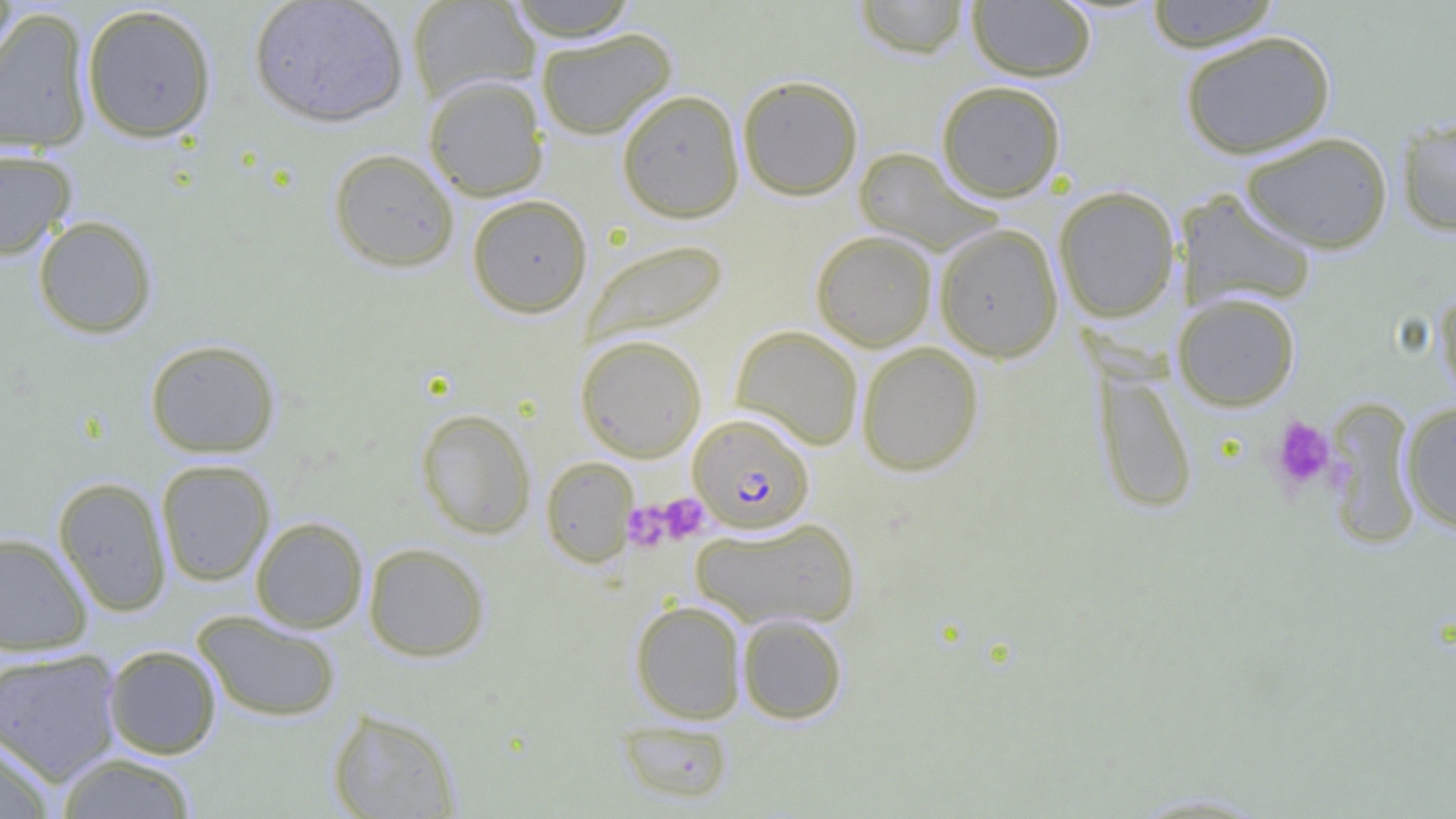 Approximate bounding boxes as (x1,y1)-(x2,y2) corner pairs in pixels. Uninfected red blood cell locations: (0,0)-(19,86), (248,0)-(409,127), (406,0)-(541,104), (504,0)-(640,41), (854,0)-(972,58), (1144,0)-(1283,52), (967,1)-(1096,82), (81,4)-(218,143), (1,9)-(94,154), (535,28)-(677,140), (1179,30)-(1337,159), (423,75)-(549,201), (737,75)-(863,201), (936,80)-(1066,202), (616,89)-(745,222), (1396,116)-(1456,236), (1240,132)-(1393,253), (853,146)-(1002,255), (0,148)-(78,259), (328,148)-(459,273), (1053,186)-(1180,323), (1175,188)-(1318,312), (467,194)-(593,318), (32,215)-(158,339), (933,223)-(1064,363), (811,230)-(937,351), (581,239)-(728,346), (1434,283)-(1456,410), (1173,292)-(1301,411), (731,325)-(864,451), (575,334)-(707,462), (144,338)-(281,458), (857,342)-(984,476), (1093,365)-(1198,515), (1325,399)-(1422,546), (1399,401)-(1456,535), (415,408)-(536,539), (541,456)-(639,568), (156,458)-(275,586), (53,476)-(172,616), (250,516)-(369,633), (690,516)-(860,631), (0,532)-(93,656), (363,542)-(490,662), (630,599)-(747,724), (192,610)-(342,723), (737,613)-(848,724), (103,645)-(222,759), (0,648)-(123,785), (327,707)-(461,818), (616,720)-(735,805), (0,737)-(56,819), (55,753)-(199,818). Plasmodium falciparum-infected red blood cell locations: (688,414)-(814,534). Platelet locations: (1270,416)-(1336,493), (659,493)-(709,543), (622,501)-(672,552). Slide-level diagnosis: Plasmodium falciparum. Thin blood smear. Captured at 1000x magnification. Light microscopy. Single field of view. Image is 1456×819 pixels.